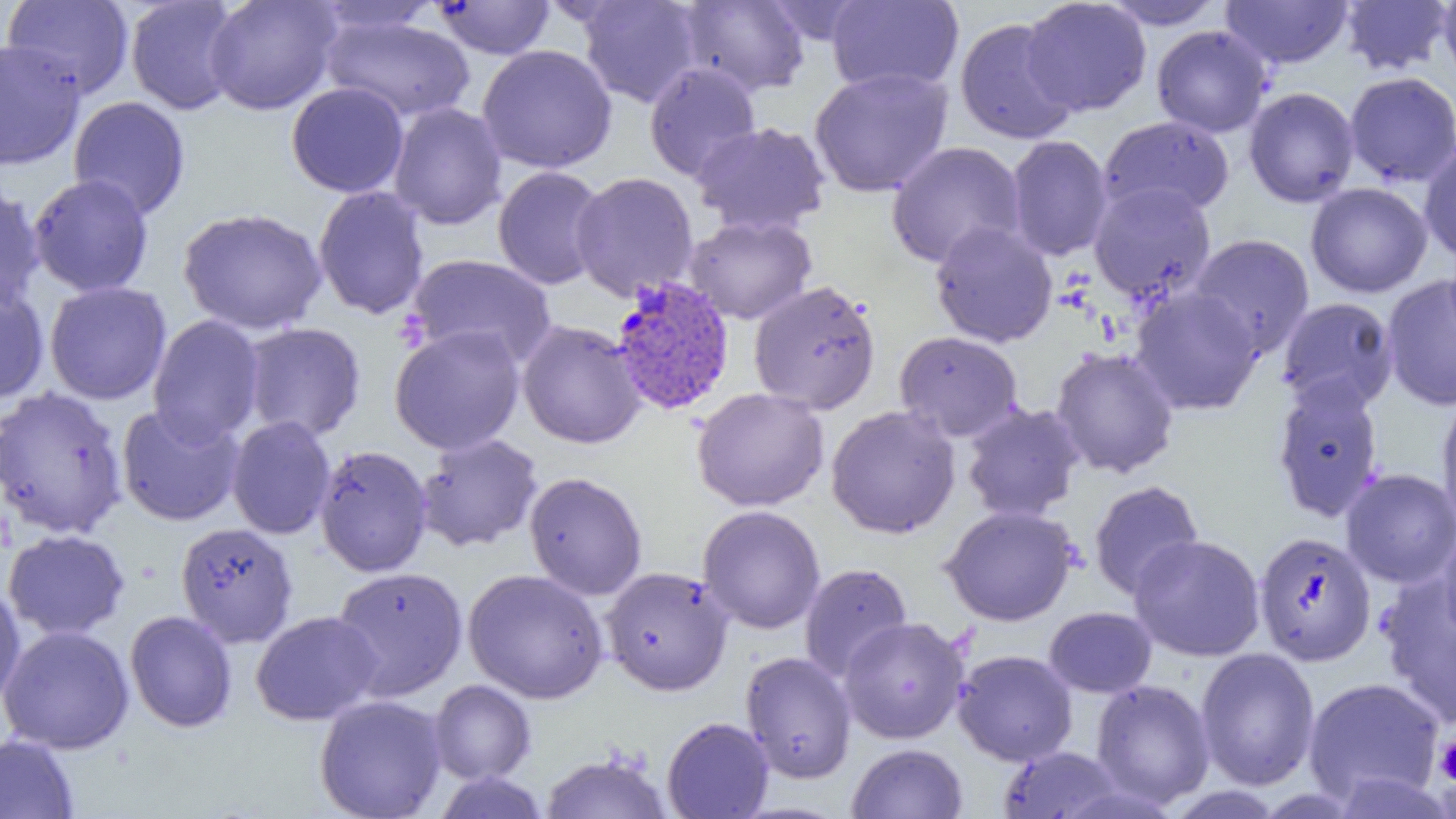
slide-level diagnosis = Plasmodium vivax
image size = 1456×819 pixels
Plasmodium vivax-infected red blood cell locations = approximate bounding boxes as named x1/y1/x2/y2 corners in pixels: (x1=608, y1=276, x2=736, y2=416)
modality = optical microscopy
preparation = thin blood film
field of view = single
uninfected red blood cell locations = approximate bounding boxes as named x1/y1/x2/y2 corners in pixels: (x1=2, y1=0, x2=135, y2=99), (x1=204, y1=0, x2=342, y2=115), (x1=577, y1=0, x2=704, y2=108), (x1=826, y1=0, x2=964, y2=96), (x1=1221, y1=0, x2=1354, y2=69), (x1=1339, y1=0, x2=1453, y2=76), (x1=1437, y1=0, x2=1456, y2=89), (x1=125, y1=1, x2=244, y2=115), (x1=309, y1=1, x2=444, y2=39), (x1=431, y1=1, x2=555, y2=59), (x1=677, y1=1, x2=811, y2=97), (x1=1021, y1=1, x2=1152, y2=116), (x1=1100, y1=1, x2=1227, y2=30), (x1=320, y1=13, x2=475, y2=123), (x1=955, y1=17, x2=1080, y2=145), (x1=1151, y1=25, x2=1273, y2=137), (x1=0, y1=38, x2=86, y2=171), (x1=477, y1=44, x2=617, y2=173), (x1=644, y1=62, x2=761, y2=183), (x1=809, y1=67, x2=953, y2=198), (x1=1343, y1=72, x2=1456, y2=187), (x1=285, y1=82, x2=409, y2=198), (x1=1243, y1=87, x2=1360, y2=208), (x1=68, y1=95, x2=191, y2=219), (x1=388, y1=102, x2=507, y2=230), (x1=1098, y1=116, x2=1235, y2=219), (x1=691, y1=121, x2=831, y2=236), (x1=1006, y1=135, x2=1113, y2=261), (x1=886, y1=141, x2=1026, y2=269), (x1=1418, y1=144, x2=1456, y2=264), (x1=492, y1=165, x2=609, y2=290), (x1=571, y1=171, x2=699, y2=301), (x1=28, y1=174, x2=154, y2=297), (x1=0, y1=181, x2=46, y2=312), (x1=1088, y1=182, x2=1217, y2=304), (x1=1305, y1=182, x2=1433, y2=298), (x1=312, y1=186, x2=430, y2=320), (x1=177, y1=207, x2=328, y2=335), (x1=684, y1=214, x2=817, y2=324), (x1=929, y1=221, x2=1059, y2=348), (x1=1189, y1=234, x2=1315, y2=358), (x1=406, y1=254, x2=557, y2=368), (x1=1381, y1=274, x2=1456, y2=412), (x1=748, y1=280, x2=882, y2=415), (x1=44, y1=281, x2=172, y2=405), (x1=0, y1=283, x2=49, y2=405), (x1=1129, y1=286, x2=1264, y2=415), (x1=1277, y1=297, x2=1399, y2=413), (x1=147, y1=315, x2=266, y2=445), (x1=516, y1=320, x2=647, y2=449), (x1=241, y1=321, x2=366, y2=443), (x1=388, y1=324, x2=526, y2=455), (x1=894, y1=331, x2=1024, y2=442), (x1=1050, y1=346, x2=1179, y2=479), (x1=1271, y1=380, x2=1385, y2=523), (x1=0, y1=386, x2=129, y2=540), (x1=691, y1=387, x2=829, y2=512), (x1=1436, y1=392, x2=1456, y2=535), (x1=961, y1=402, x2=1086, y2=522), (x1=116, y1=403, x2=245, y2=527), (x1=825, y1=405, x2=961, y2=539), (x1=226, y1=415, x2=336, y2=540), (x1=416, y1=433, x2=543, y2=552), (x1=314, y1=444, x2=433, y2=578), (x1=1340, y1=468, x2=1456, y2=589), (x1=523, y1=472, x2=648, y2=600), (x1=1088, y1=480, x2=1204, y2=600), (x1=697, y1=505, x2=826, y2=634), (x1=940, y1=505, x2=1080, y2=626), (x1=175, y1=522, x2=298, y2=647), (x1=1436, y1=523, x2=1456, y2=646), (x1=2, y1=529, x2=130, y2=640), (x1=1253, y1=531, x2=1376, y2=666), (x1=1128, y1=534, x2=1266, y2=661), (x1=799, y1=563, x2=913, y2=682), (x1=329, y1=566, x2=469, y2=701), (x1=601, y1=566, x2=734, y2=696), (x1=463, y1=568, x2=609, y2=704), (x1=1375, y1=575, x2=1456, y2=727), (x1=0, y1=582, x2=26, y2=709), (x1=1044, y1=606, x2=1157, y2=698), (x1=124, y1=610, x2=237, y2=733), (x1=250, y1=610, x2=382, y2=725), (x1=838, y1=616, x2=969, y2=744), (x1=0, y1=624, x2=134, y2=754), (x1=1195, y1=648, x2=1321, y2=790), (x1=952, y1=649, x2=1078, y2=766), (x1=740, y1=651, x2=857, y2=783), (x1=1302, y1=676, x2=1445, y2=807), (x1=428, y1=679, x2=537, y2=784), (x1=1090, y1=679, x2=1215, y2=809), (x1=314, y1=695, x2=448, y2=819), (x1=661, y1=716, x2=774, y2=818), (x1=0, y1=734, x2=79, y2=819), (x1=847, y1=743, x2=968, y2=818), (x1=997, y1=746, x2=1127, y2=818), (x1=540, y1=751, x2=673, y2=818), (x1=431, y1=771, x2=552, y2=818)
platelet locations = approximate bounding boxes as named x1/y1/x2/y2 corners in pixels: (x1=1433, y1=734, x2=1456, y2=787)
magnification = 1000x